Comment on the morphology of the red blood cells.
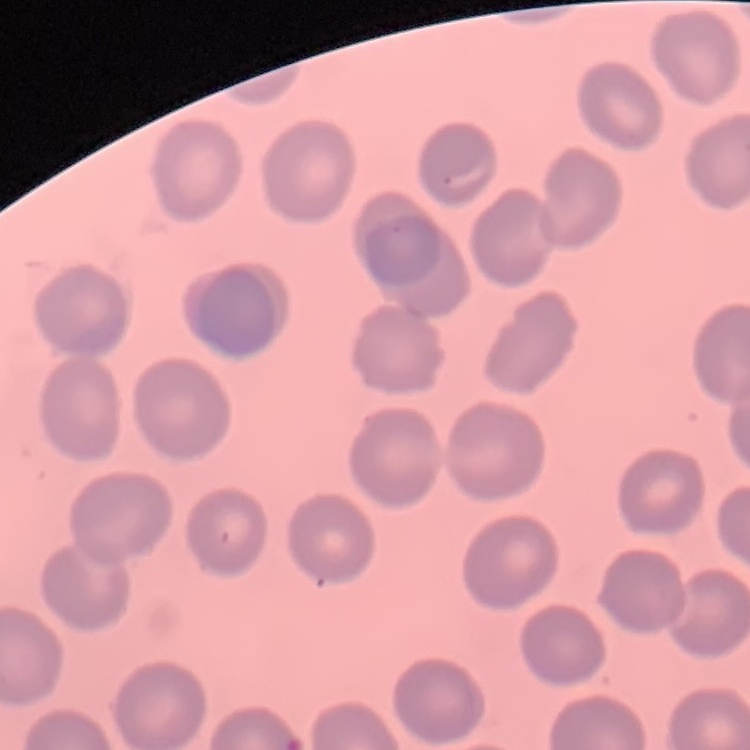

They show no rouleaux formation.

stain: Field's or Giemsa
preparation: thin peripheral smear
image_type: square crop of a larger photomicrograph